Name the parasite shown.
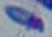
This is Toxoplasma gondii.

magnification: 1000x
modality: micrograph